Comment on the morphology of the red blood cells.
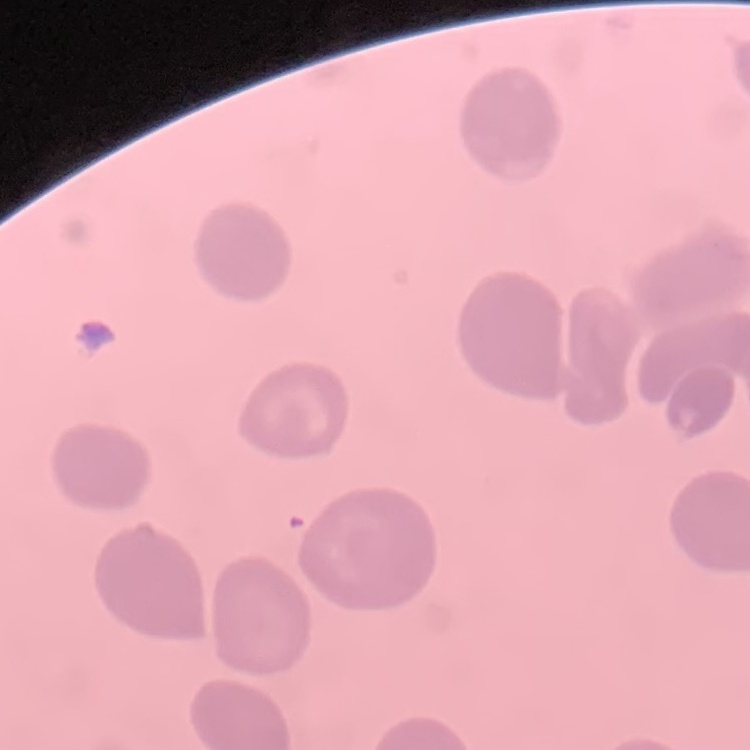

They show no rouleaux formation.

Summary:
  - Image type: square crop of a larger photomicrograph
  - Stain: Field's or Giemsa
  - Preparation: thin blood film